Name the parasite shown.
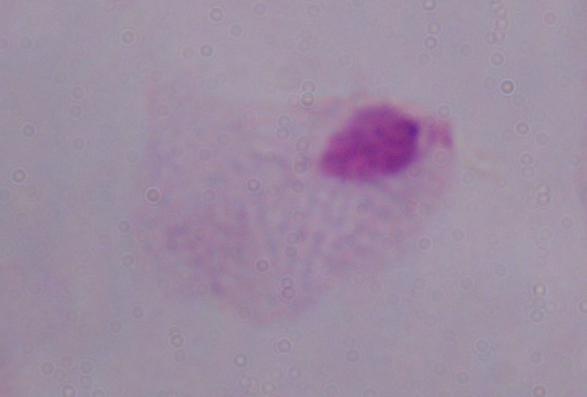

This is a trichomonad.

Summary:
  - Modality: micrograph
  - Magnification: 1000x